Assess this cell for malaria.
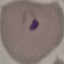

Parasitized.

Thin blood film. Cell patch, automatically extracted from a larger field of view and resized to 64 × 64 pixels. Acquired by smartphone through the microscope eyepiece. Giemsa stain.